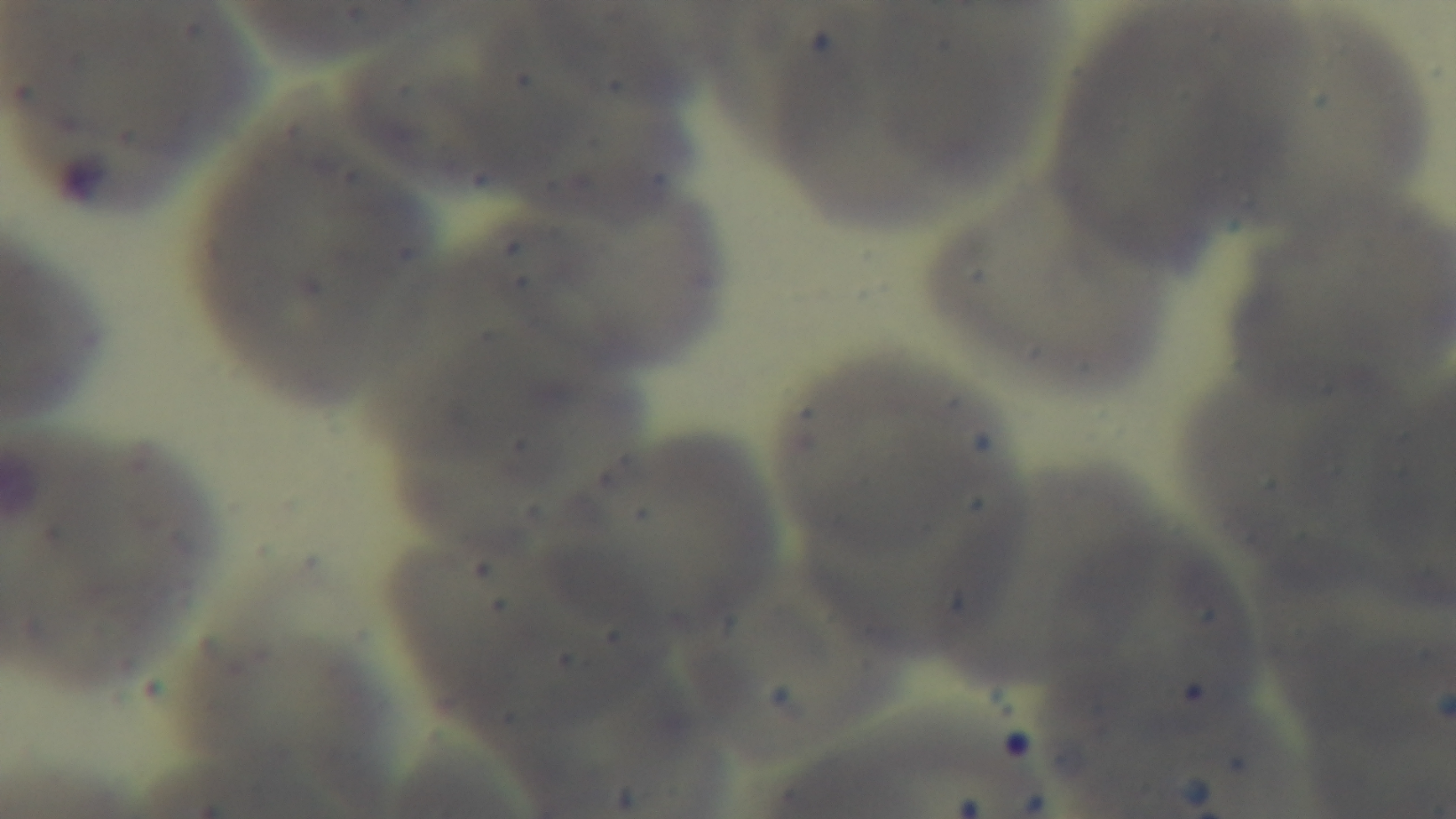

Giemsa-stained. 100x oil-immersion objective. Photomicrograph. Single field of view. Mounted 4K digital camera. Preparation: thin smear. Malaria status: uninfected.